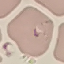

Summary:
  - Result: malaria parasites detected
  - Preparation: thin blood smear
  - Stain: Giemsa
  - Image type: cell patch, automatically extracted from a larger field of view and resized to 64 × 64 pixels
  - Capture: smartphone through the microscope eyepiece